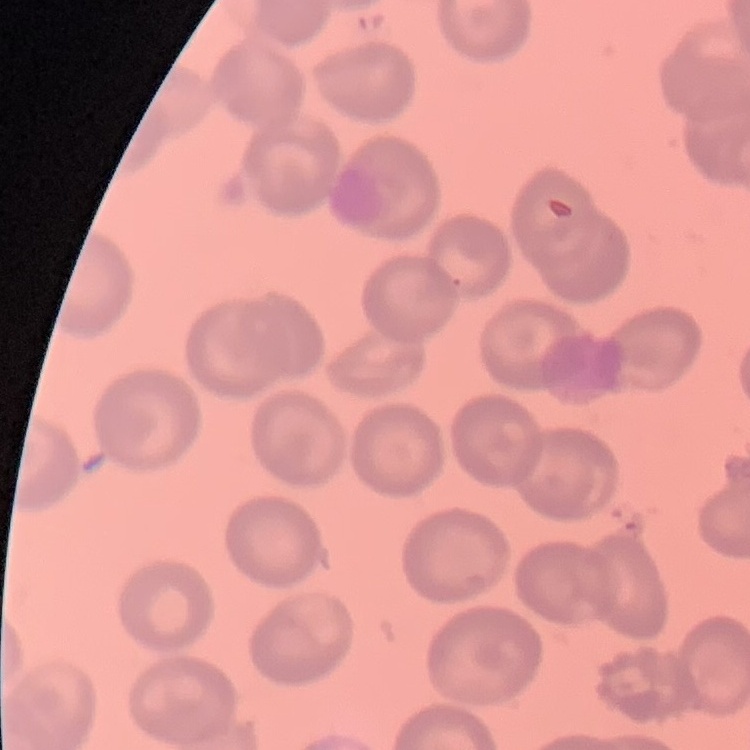

red blood cell morphology = no rouleaux formation
preparation = thin blood smear
stain = Field's or Giemsa
image type = one tile cut from a larger photomicrograph